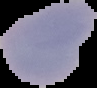
image_type: cell region segmented out of the field of view; surrounding area masked to black
image_size: 97×88 pixels
result: negative for Plasmodium parasites
preparation: thin blood smear